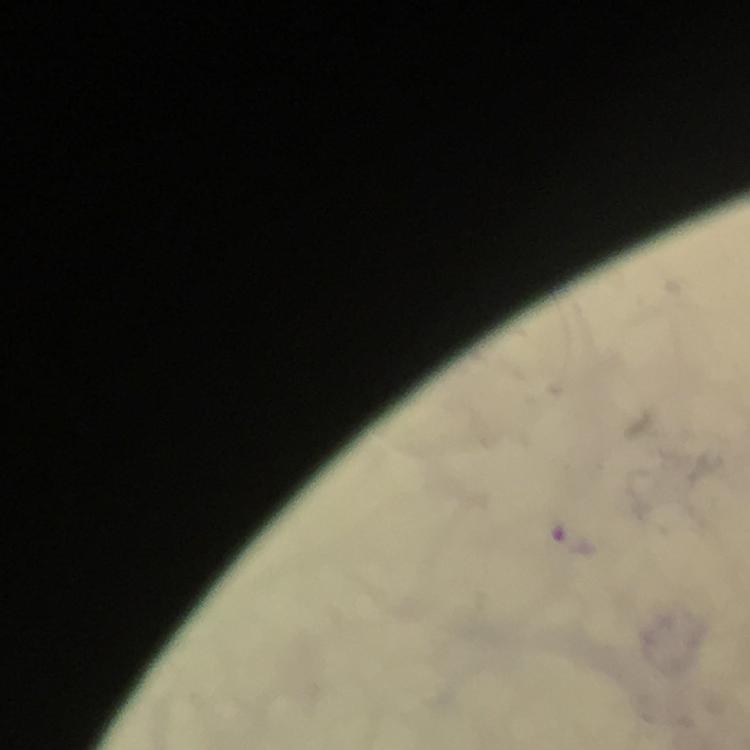

Approximate centers as (x, y) in pixels.
Summary:
  - Malaria parasite locations: (571, 538)
  - Image size: 750×750 pixels
  - Preparation: thick blood smear
  - Immersion oil: applied
  - Magnification: 100x
  - Capture: smartphone mounted on the microscope
  - Context: from a diagnostic examination for malaria
  - Stain: Giemsa
  - Cropped from: one field of view